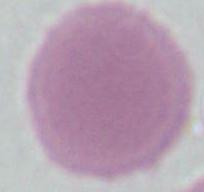 Captured at 1000x magnification. Photomicrograph. An erythrocyte is shown.